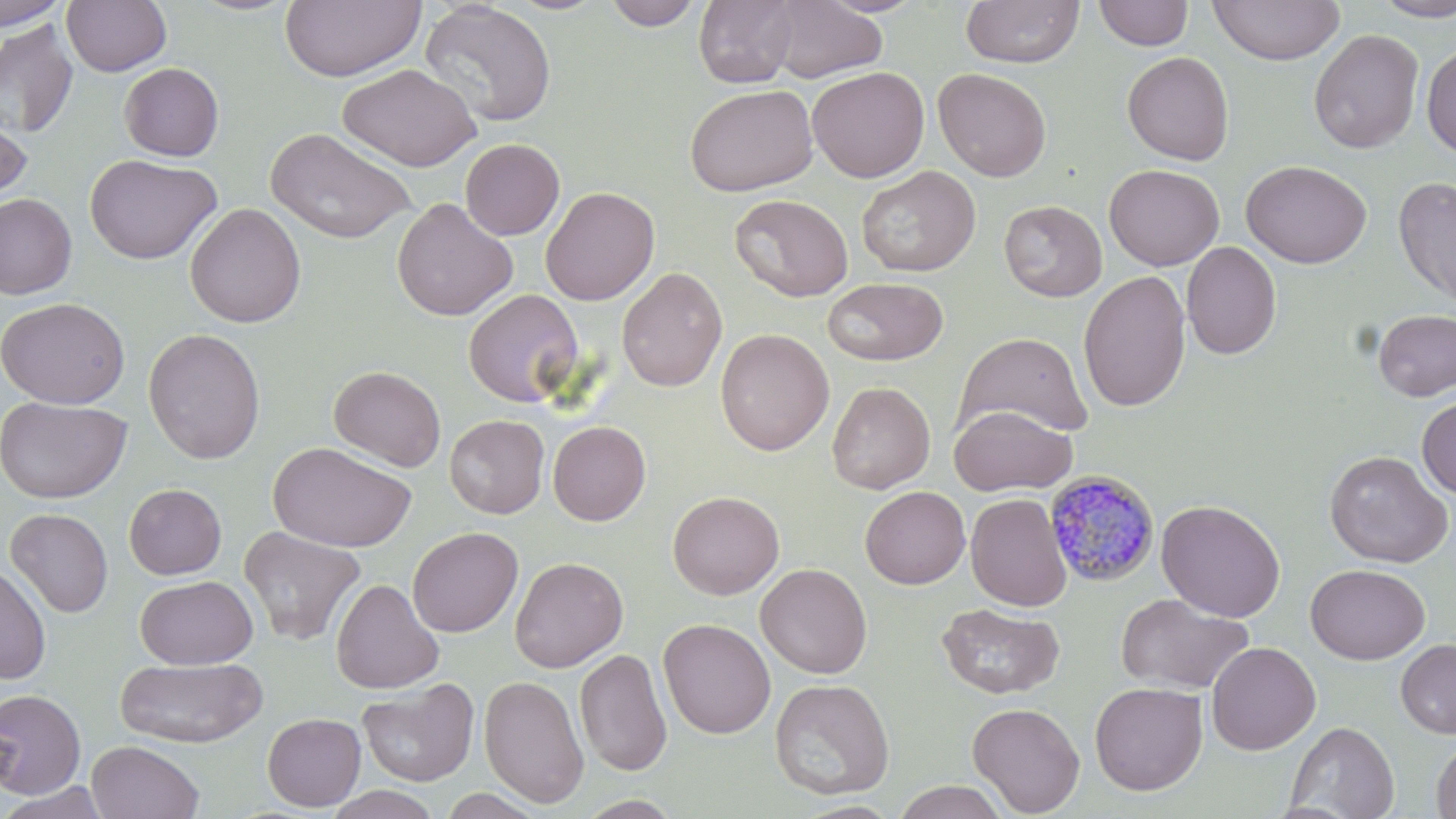
slide_level_diagnosis: Plasmodium malariae
magnification: 1000x
uninfected_red_blood_cell_locations: 'approximate bounding boxes as [x1, y1, x2, y2] in pixels: [0, 0, 70, 31], [61, 0, 172, 76], [602, 0, 704, 30], [693, 0, 799, 89], [815, 0, 927, 17], [960, 0, 1085, 68], [1208, 0, 1345, 65], [1373, 0, 1456, 21], [280, 1, 426, 82], [418, 1, 557, 129], [767, 1, 888, 84], [1093, 1, 1193, 50], [0, 19, 79, 141], [1308, 29, 1425, 154], [1421, 43, 1456, 157], [1121, 51, 1235, 165], [119, 62, 224, 161], [339, 64, 480, 171], [807, 66, 929, 183], [933, 68, 1052, 181], [684, 84, 818, 196], [1, 106, 33, 206], [266, 126, 418, 245], [460, 138, 565, 240], [85, 153, 222, 265], [1241, 159, 1372, 268], [1104, 163, 1224, 271], [856, 165, 980, 278], [1393, 177, 1456, 310], [540, 186, 660, 305], [0, 192, 77, 300], [730, 193, 853, 302], [391, 197, 518, 321], [998, 200, 1107, 302], [185, 203, 306, 328], [1181, 241, 1282, 360], [616, 267, 728, 392], [1078, 269, 1191, 413], [822, 277, 948, 365], [463, 289, 585, 407], [1, 296, 130, 409], [1372, 308, 1456, 402], [142, 327, 266, 464], [715, 328, 834, 455], [956, 331, 1093, 437], [329, 365, 446, 471], [826, 381, 935, 494], [1417, 395, 1456, 500], [0, 396, 131, 504], [949, 404, 1077, 496], [444, 414, 549, 519], [548, 421, 651, 526], [267, 441, 416, 551], [1324, 450, 1453, 567], [124, 483, 226, 579], [860, 486, 970, 588], [667, 490, 784, 600], [965, 493, 1072, 612], [1156, 499, 1286, 622], [5, 508, 113, 618], [239, 526, 366, 646], [408, 526, 524, 637], [509, 556, 628, 673], [0, 562, 51, 685], [755, 563, 872, 678], [1305, 563, 1429, 665], [135, 575, 257, 669], [330, 578, 445, 693], [1115, 592, 1254, 695], [936, 602, 1064, 699], [658, 618, 776, 739], [1395, 638, 1456, 739], [1206, 641, 1321, 755], [574, 647, 673, 777], [114, 656, 268, 747], [478, 674, 589, 808], [357, 678, 479, 787], [770, 678, 895, 800], [1089, 681, 1208, 796], [0, 689, 86, 798], [967, 701, 1085, 816], [262, 712, 366, 811], [1284, 720, 1400, 818], [1430, 737, 1456, 819], [86, 740, 204, 819], [892, 780, 1009, 818], [0, 782, 113, 818], [324, 786, 442, 819], [435, 788, 547, 819], [573, 794, 685, 818]'
preparation: thin blood smear
stain: May-Grünwald-Giemsa
image_size: 1456×819 pixels
field_of_view: one of a larger specimen
plasmodium_malariae_infected_red_blood_cell_locations: 'approximate bounding boxes as [x1, y1, x2, y2] in pixels: [1045, 468, 1161, 587]'
modality: light microscopy